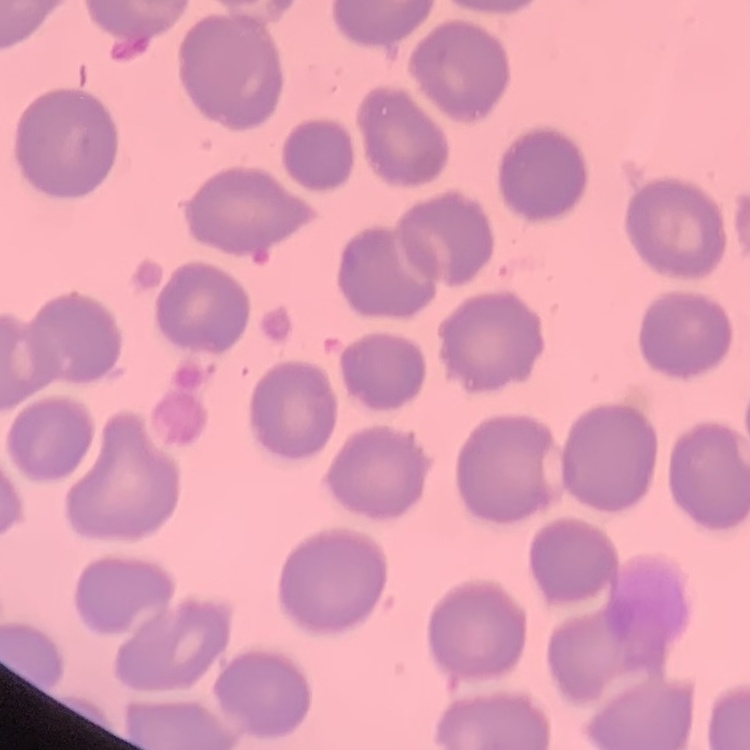

The erythrocytes show no rouleaux formation. Stained with either Field's or Giemsa. Square crop of a larger photomicrograph. Thin blood film.